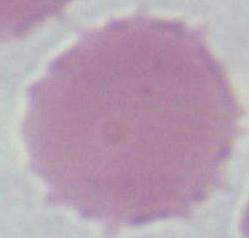
magnification = 1000x
modality = photomicrograph
identification = red blood cell